Classify this cell by malaria status.
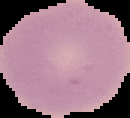

It is uninfected.

{
  "image_type": "segmented cell region on a black background",
  "preparation": "thin blood smear",
  "image_size": "130×118 pixels"
}